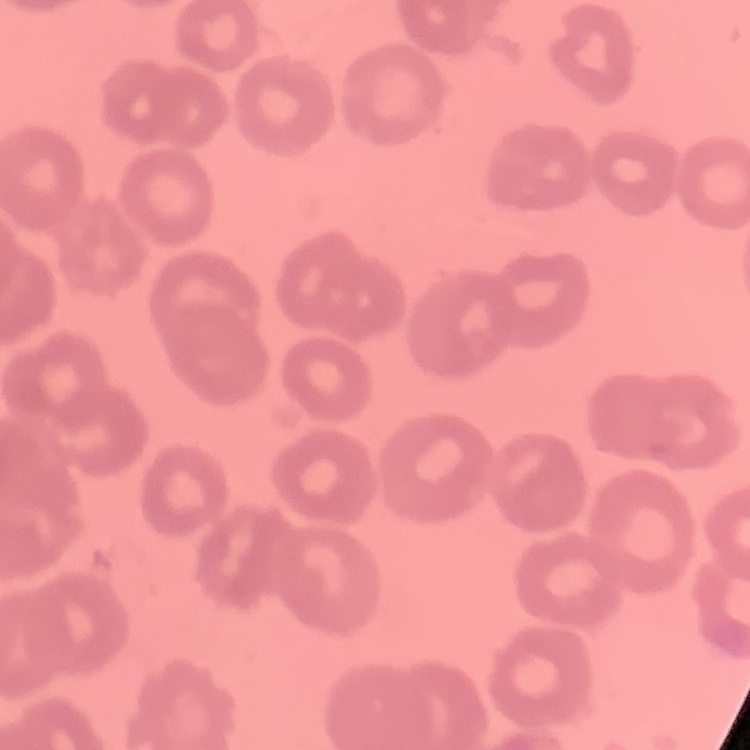 The red blood cells show no rouleaux formation. Thin blood film. Square crop of a larger photomicrograph. Field's or Giemsa stain.